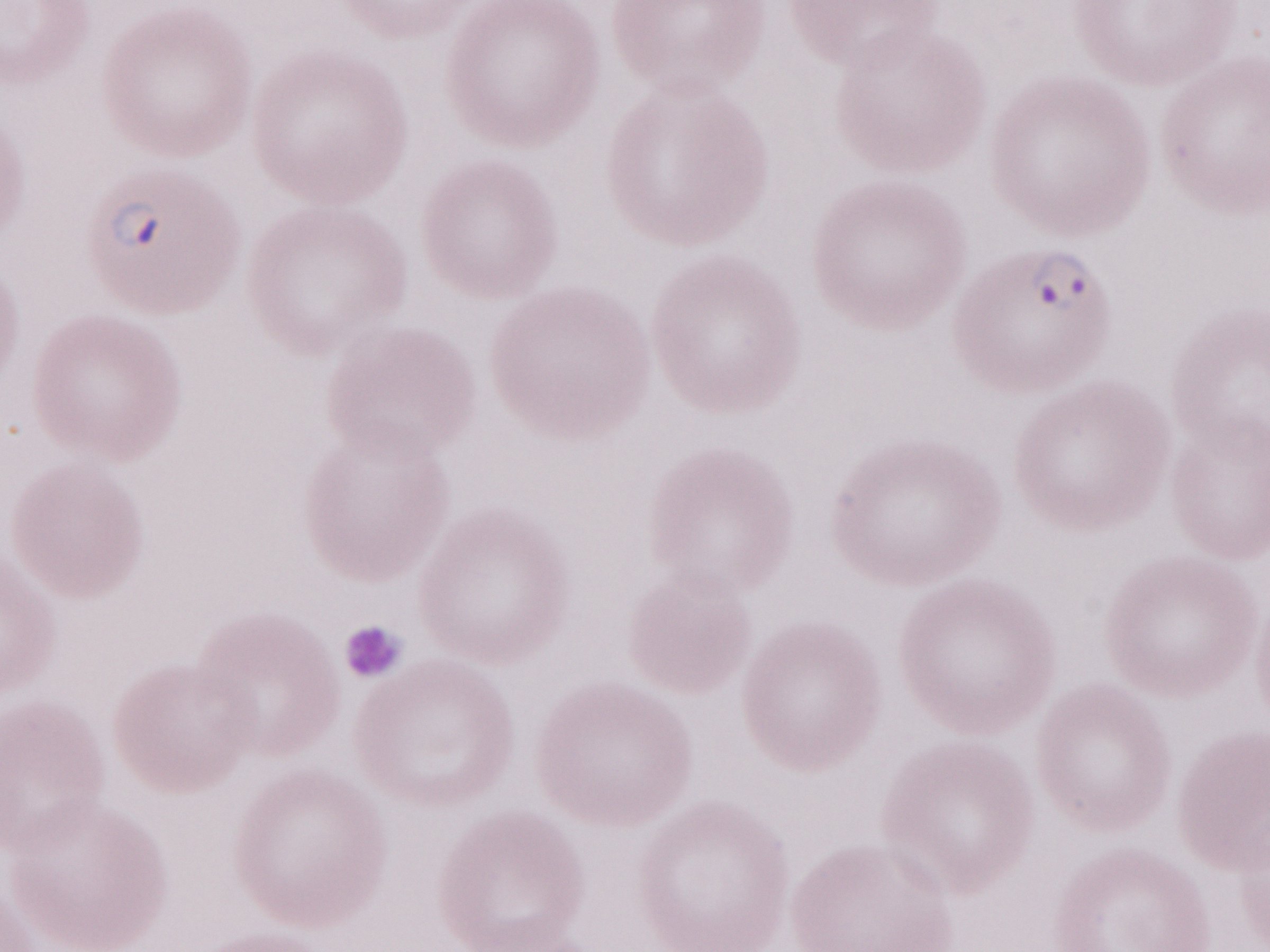 Image is 1270×952 pixels. Malaria diagnosis (patient-level): positive. Thin blood film. May-Grünwald-Giemsa stain. One field of this slide. Olympus BX43 microscope, Olympus DP73 camera. 1,000x magnification.